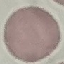

Result: no malaria parasites seen. Automatically extracted cell patch, resized to 64 × 64 pixels. Giemsa-stained preparation. Thin blood smear. Acquired by smartphone through the microscope eyepiece.